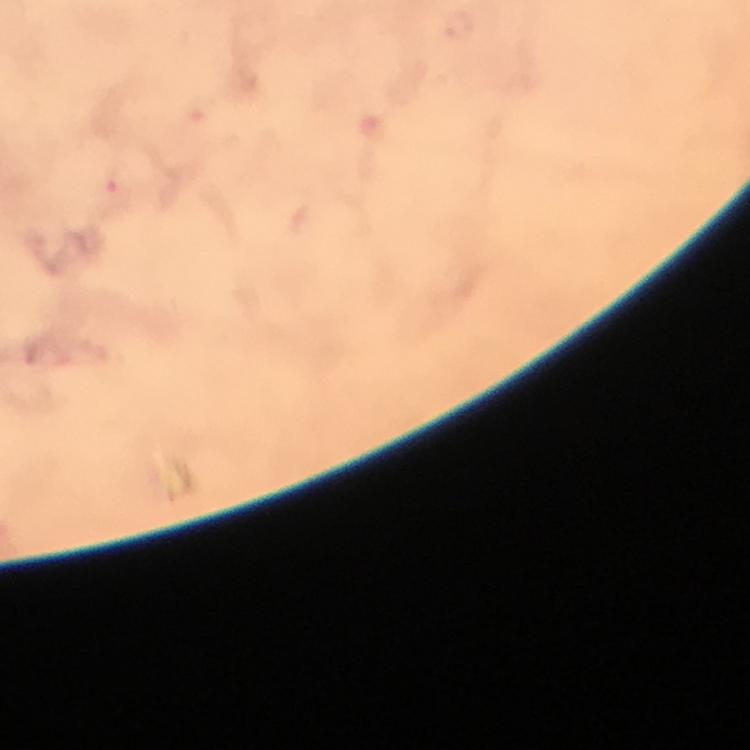 Approximate object centers, in pixels from the top-left corner. Plasmodium parasite locations: (x=117, y=183). At 100x magnification. Giemsa-stained preparation. Thick blood smear. From a malaria diagnostic workup. A crop from one field of view. Image is 750×750 pixels. Immersion oil applied. Smartphone photograph taken through a microscope.